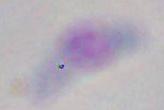 Captured at 1000x magnification. Micrograph. Toxoplasma gondii is seen.